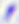 Toxoplasma gondii is seen. 400x magnification. Photomicrograph.